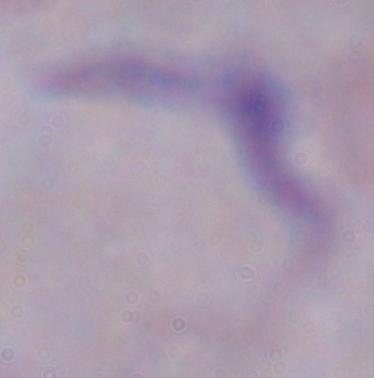
magnification = 1000x
modality = photomicrograph
identification = trypanosome